Locate and identify every blood parasite.
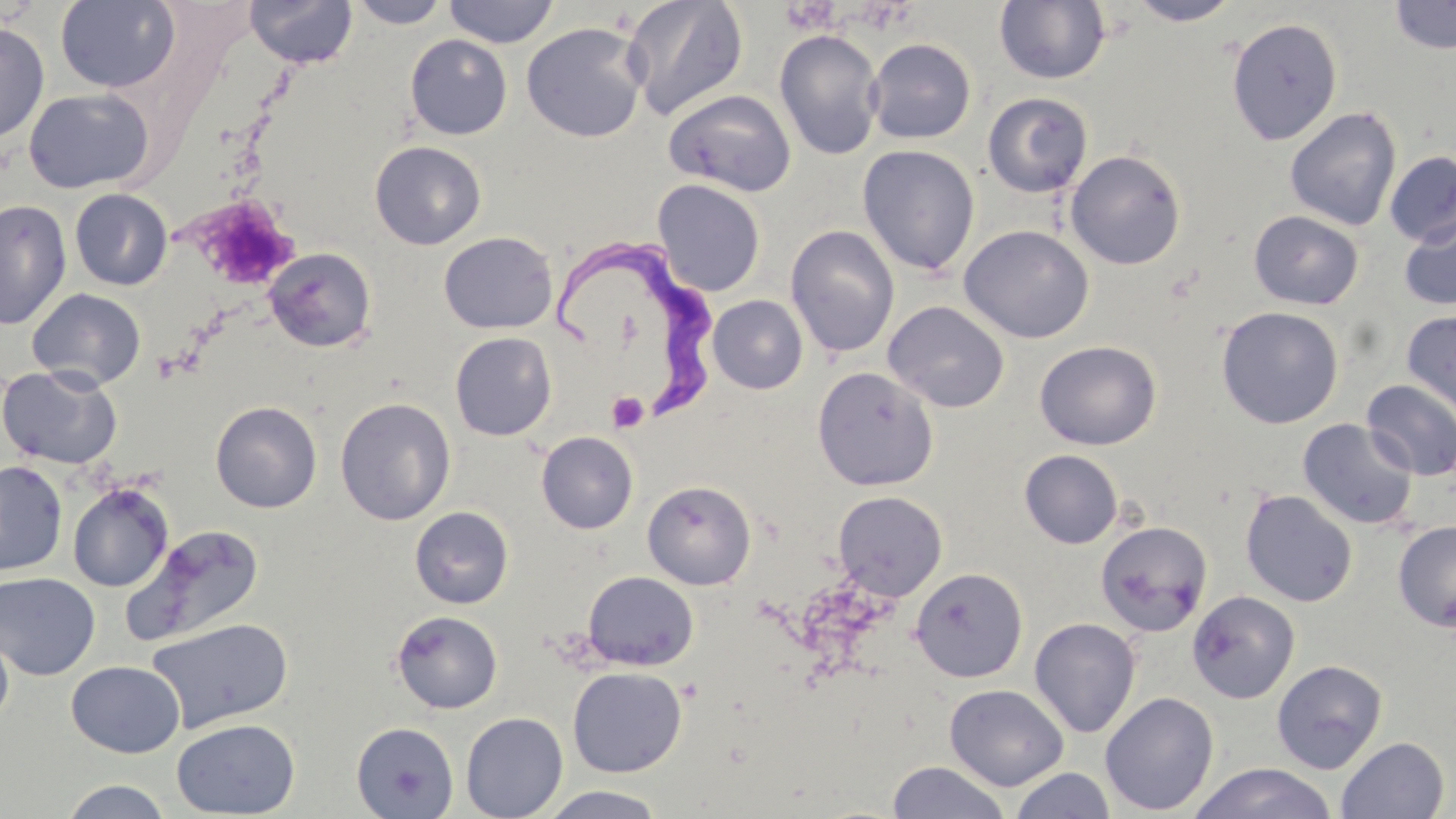

Approximate bounding boxes as (x1, y1, x2, y2) in pixels.
Trypanosoma brucei: (562, 231, 721, 420).
No Plasmodium falciparum, Plasmodium ovale, Plasmodium malariae, Plasmodium vivax, or Babesia divergens observed.

{
  "slide_level_diagnosis": "Trypanosoma brucei",
  "modality": "optical microscopy",
  "platelet_locations": "approximate bounding boxes as (x1, y1, x2, y2) in pixels: (781, 2, 841, 34), (212, 211, 292, 273), (607, 392, 649, 432)",
  "uninfected_red_blood_cell_locations": "approximate bounding boxes as (x1, y1, x2, y2) in pixels: (55, 0, 181, 92), (245, 0, 358, 68), (348, 0, 451, 28), (443, 0, 560, 48), (622, 0, 748, 121), (994, 0, 1110, 85), (1126, 0, 1241, 26), (1388, 0, 1455, 55), (1226, 17, 1343, 145), (0, 20, 50, 144), (522, 21, 647, 143), (774, 29, 884, 160), (405, 34, 513, 140), (865, 38, 976, 144), (23, 87, 155, 194), (663, 88, 796, 197), (983, 93, 1092, 198), (1284, 106, 1402, 230), (370, 141, 487, 250), (857, 144, 980, 275), (1065, 149, 1186, 270), (1384, 151, 1456, 247), (652, 179, 766, 296), (69, 188, 173, 290), (0, 200, 71, 330), (1249, 210, 1364, 310), (1399, 212, 1456, 311), (786, 224, 900, 358), (959, 224, 1094, 343), (439, 231, 558, 334), (263, 247, 377, 352), (27, 288, 146, 390), (708, 295, 807, 394), (883, 300, 1010, 413), (1216, 306, 1344, 429), (1401, 310, 1456, 426), (450, 332, 557, 441), (1034, 340, 1162, 450), (0, 365, 123, 470), (812, 367, 939, 491), (1361, 379, 1456, 480), (335, 397, 455, 525), (210, 401, 322, 513), (1297, 417, 1419, 530), (536, 431, 638, 534), (1019, 449, 1123, 548), (0, 460, 68, 576), (643, 480, 756, 590), (68, 482, 173, 592), (1240, 489, 1358, 607), (832, 490, 948, 601), (410, 506, 513, 609), (1096, 520, 1213, 636), (1393, 521, 1456, 632), (124, 524, 265, 645), (909, 567, 1028, 683), (581, 571, 699, 670), (0, 572, 101, 680), (1187, 590, 1300, 704), (391, 610, 503, 713), (146, 617, 295, 733), (1029, 617, 1142, 738), (0, 623, 14, 727), (1271, 659, 1388, 774), (66, 660, 185, 757), (567, 666, 687, 778), (944, 684, 1069, 790), (1100, 691, 1219, 815), (460, 712, 568, 819), (171, 718, 300, 818), (350, 721, 459, 818), (1335, 736, 1450, 819), (886, 760, 1012, 819), (1187, 762, 1338, 819), (1009, 767, 1116, 818), (59, 778, 173, 818), (538, 786, 667, 819)",
  "field_of_view": "single",
  "preparation": "thin blood smear",
  "image_size": "1456×819 pixels",
  "stain": "May-Grünwald-Giemsa",
  "magnification": "1000x"
}